Report the malaria status of this cell.
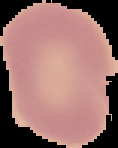

It is uninfected.

Image is 118×148 pixels. Segmented cell region on a black background. From a thin blood smear.